Identify the parasite.
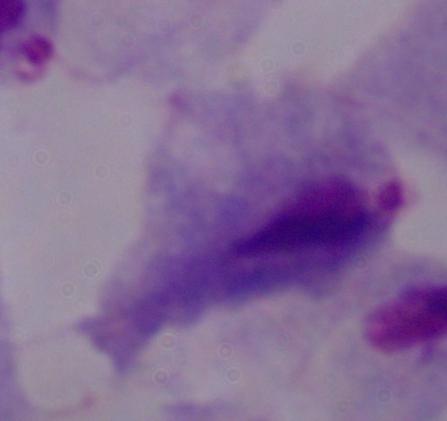
A trichomonad.

magnification = 1000x
modality = micrograph